Outline each blood parasite and name the species.
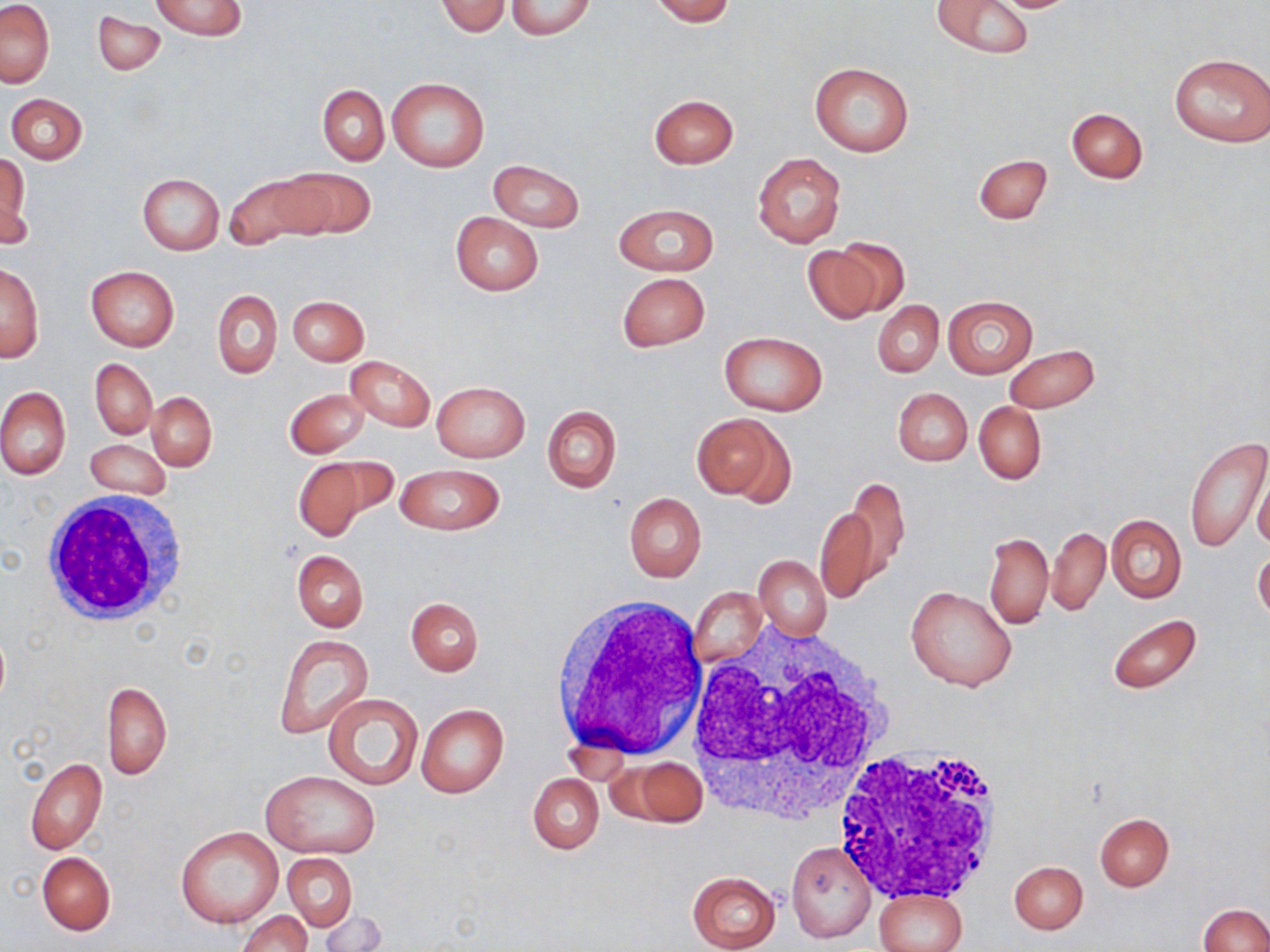
No blood parasites seen.

Approximate bounding boxes as (x1,y1)-(x2,y2) corner pairs in pixels. White blood cell locations: (37,493)-(193,629), (550,594)-(709,763), (682,622)-(898,823), (832,742)-(1004,903). Uninfected red blood cell locations: (151,0)-(247,42), (505,0)-(597,42), (650,0)-(735,24), (932,0)-(1037,60), (986,0)-(1086,13), (0,1)-(53,87), (437,1)-(510,37), (94,11)-(164,75), (1170,53)-(1269,146), (808,62)-(915,156), (388,77)-(489,171), (318,85)-(389,166), (5,93)-(88,163), (649,94)-(739,169), (1066,108)-(1147,183), (1,151)-(31,246), (752,152)-(845,248), (974,154)-(1051,224), (488,160)-(584,232), (279,167)-(375,239), (224,172)-(324,249), (136,173)-(224,255), (614,203)-(718,276), (450,212)-(543,295), (801,241)-(897,324), (1,262)-(44,361), (85,266)-(179,351), (617,272)-(710,352), (213,289)-(282,380), (288,295)-(368,365), (943,296)-(1038,378), (873,301)-(943,376), (720,332)-(825,416), (1003,345)-(1100,414), (346,356)-(435,432), (91,359)-(156,439), (431,380)-(530,462), (0,386)-(70,479), (284,387)-(371,458), (892,387)-(972,467), (147,392)-(216,471), (973,402)-(1047,484), (542,405)-(621,493), (694,412)-(789,501), (1184,437)-(1269,553), (85,440)-(172,500), (289,457)-(381,543), (394,463)-(505,536), (1253,471)-(1270,553), (838,476)-(909,588), (623,492)-(706,582), (815,503)-(882,606), (1106,514)-(1186,603), (1047,527)-(1109,617), (984,531)-(1053,629), (292,550)-(368,632), (1253,551)-(1270,623), (753,555)-(831,640), (905,586)-(1017,692), (690,588)-(766,668), (406,598)-(483,676), (1107,613)-(1201,693), (274,634)-(373,738), (101,681)-(172,780), (321,691)-(425,792), (416,703)-(508,798), (25,757)-(107,854), (621,757)-(707,826), (261,770)-(382,860), (528,774)-(603,853), (1094,813)-(1174,890), (175,826)-(284,928), (786,840)-(877,943), (37,852)-(115,935), (284,852)-(358,932), (1009,861)-(1088,934), (686,871)-(782,951), (872,885)-(970,951), (1199,904)-(1269,952), (316,910)-(388,951), (237,911)-(312,952). Slide-level diagnosis: no evidence of blood parasites. Thin blood smear. 1000x magnification. Light microscopy. Single field of view. Image is 1270×952 pixels. May-Grünwald-Giemsa stain.